State the blood parasite species.
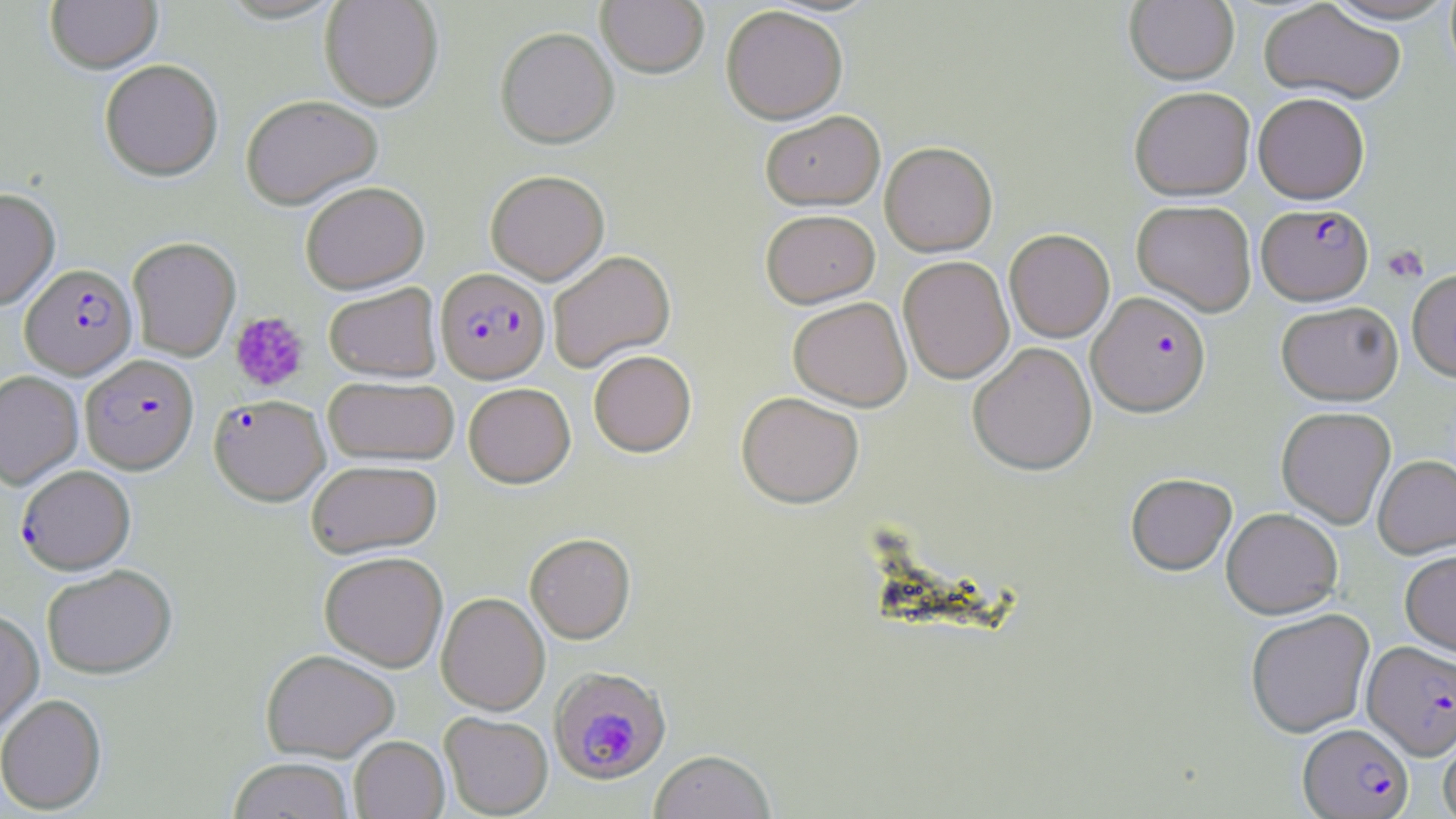

Plasmodium falciparum.

Approximate bounding boxes as [x1, y1, x2, y2] in pixels. Plasmodium falciparum-infected red blood cell locations: [1259, 202, 1376, 303], [20, 263, 137, 379], [435, 267, 550, 382], [1088, 291, 1210, 415], [80, 354, 198, 473], [209, 394, 330, 505], [17, 465, 135, 574], [1363, 641, 1456, 759], [550, 665, 672, 784], [1299, 722, 1413, 817]. Platelet locations: [1382, 245, 1428, 284], [230, 311, 309, 391]. Uninfected red blood cell locations: [45, 0, 162, 74], [1321, 0, 1456, 24], [320, 1, 443, 110], [596, 1, 709, 78], [1125, 1, 1239, 84], [1259, 1, 1406, 104], [721, 6, 848, 124], [495, 26, 619, 148], [99, 59, 223, 181], [1129, 86, 1255, 200], [1253, 92, 1369, 204], [241, 94, 383, 209], [761, 110, 885, 210], [880, 141, 997, 256], [486, 169, 609, 284], [301, 181, 429, 294], [0, 187, 60, 310], [1132, 200, 1257, 316], [761, 209, 880, 308], [1004, 229, 1115, 342], [127, 237, 241, 361], [547, 250, 675, 372], [898, 255, 1014, 384], [1407, 269, 1456, 381], [323, 282, 442, 382], [788, 296, 912, 411], [1276, 301, 1403, 405], [968, 342, 1096, 475], [588, 350, 696, 457], [0, 371, 83, 489], [323, 375, 460, 465], [463, 382, 575, 487], [736, 391, 864, 508], [1276, 406, 1396, 528], [1373, 455, 1456, 558], [306, 459, 442, 558], [1125, 472, 1237, 575], [1221, 507, 1343, 618], [524, 532, 635, 643], [1400, 549, 1456, 655], [319, 551, 448, 671], [41, 564, 176, 679], [437, 592, 550, 714], [0, 608, 44, 734], [1245, 608, 1375, 737], [260, 648, 400, 762], [0, 694, 107, 814], [440, 711, 553, 817], [1438, 720, 1456, 819], [349, 736, 449, 819], [649, 749, 776, 819], [228, 757, 355, 819]. Thin blood film. One field of a larger specimen. Optical microscopy. Captured at 1000x magnification. Image is 1456×819 pixels. May-Grünwald-Giemsa stain.